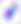

400x magnification. Micrograph. Toxoplasma gondii is shown.